State which parasite is depicted.
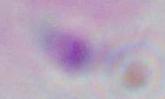

This is Toxoplasma gondii.

Micrograph. Captured at 1000x magnification.